Name the blood parasite species.
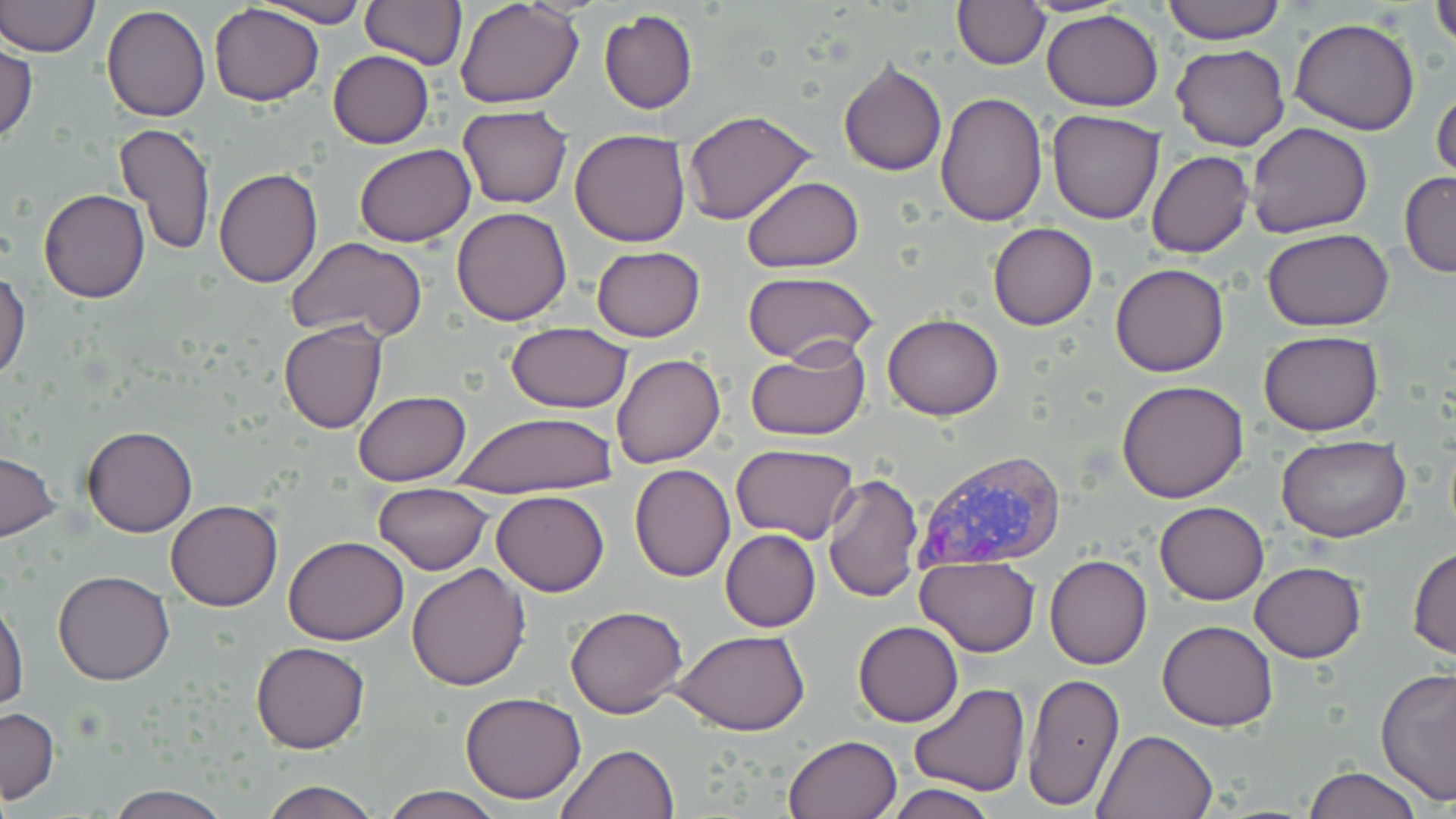
Plasmodium vivax.

Approximate bounding boxes as named x1/y1/x2/y2 corners in pixels. Plasmodium vivax-infected red blood cell locations: (x1=911, y1=447, x2=1068, y2=572). Uninfected red blood cell locations: (x1=1, y1=0, x2=100, y2=57), (x1=1160, y1=0, x2=1286, y2=44), (x1=1432, y1=0, x2=1455, y2=53), (x1=253, y1=1, x2=369, y2=27), (x1=360, y1=1, x2=467, y2=69), (x1=455, y1=1, x2=583, y2=108), (x1=951, y1=1, x2=1050, y2=71), (x1=208, y1=2, x2=324, y2=106), (x1=101, y1=4, x2=210, y2=121), (x1=599, y1=9, x2=698, y2=113), (x1=1041, y1=9, x2=1164, y2=110), (x1=1290, y1=17, x2=1420, y2=135), (x1=1, y1=42, x2=37, y2=142), (x1=1172, y1=42, x2=1291, y2=151), (x1=327, y1=49, x2=434, y2=149), (x1=838, y1=59, x2=947, y2=177), (x1=1431, y1=81, x2=1455, y2=189), (x1=935, y1=93, x2=1048, y2=227), (x1=458, y1=105, x2=573, y2=209), (x1=682, y1=109, x2=817, y2=225), (x1=1046, y1=109, x2=1165, y2=224), (x1=1245, y1=122, x2=1373, y2=240), (x1=114, y1=123, x2=216, y2=256), (x1=568, y1=128, x2=691, y2=246), (x1=354, y1=144, x2=477, y2=247), (x1=1146, y1=150, x2=1253, y2=258), (x1=212, y1=168, x2=323, y2=288), (x1=1399, y1=172, x2=1456, y2=276), (x1=741, y1=177, x2=865, y2=273), (x1=39, y1=187, x2=150, y2=304), (x1=451, y1=206, x2=572, y2=326), (x1=987, y1=222, x2=1098, y2=330), (x1=1262, y1=228, x2=1393, y2=333), (x1=283, y1=237, x2=428, y2=343), (x1=591, y1=245, x2=706, y2=342), (x1=1110, y1=263, x2=1229, y2=377), (x1=1, y1=269, x2=30, y2=381), (x1=743, y1=271, x2=877, y2=363), (x1=882, y1=315, x2=1003, y2=421), (x1=278, y1=322, x2=386, y2=435), (x1=503, y1=322, x2=633, y2=413), (x1=1257, y1=329, x2=1384, y2=437), (x1=746, y1=338, x2=872, y2=441), (x1=611, y1=352, x2=725, y2=467), (x1=1117, y1=379, x2=1249, y2=502), (x1=353, y1=390, x2=470, y2=486), (x1=447, y1=412, x2=616, y2=498), (x1=81, y1=424, x2=198, y2=537), (x1=1278, y1=436, x2=1411, y2=543), (x1=730, y1=443, x2=859, y2=544), (x1=0, y1=450, x2=60, y2=542), (x1=629, y1=464, x2=736, y2=583), (x1=821, y1=470, x2=924, y2=603), (x1=373, y1=483, x2=493, y2=575), (x1=492, y1=490, x2=609, y2=596), (x1=166, y1=500, x2=282, y2=612), (x1=1154, y1=501, x2=1269, y2=604), (x1=720, y1=529, x2=821, y2=632), (x1=283, y1=536, x2=408, y2=645), (x1=1407, y1=545, x2=1456, y2=660), (x1=915, y1=554, x2=1040, y2=655), (x1=1045, y1=555, x2=1151, y2=670), (x1=405, y1=562, x2=531, y2=691), (x1=1250, y1=562, x2=1366, y2=663), (x1=55, y1=569, x2=174, y2=684), (x1=1, y1=594, x2=28, y2=710), (x1=565, y1=603, x2=689, y2=719), (x1=853, y1=620, x2=962, y2=727), (x1=1157, y1=620, x2=1278, y2=731), (x1=673, y1=630, x2=810, y2=735), (x1=250, y1=641, x2=369, y2=754), (x1=1376, y1=666, x2=1455, y2=802), (x1=1023, y1=672, x2=1125, y2=810), (x1=909, y1=683, x2=1031, y2=796), (x1=460, y1=691, x2=585, y2=803), (x1=0, y1=707, x2=58, y2=804), (x1=1092, y1=728, x2=1219, y2=818), (x1=784, y1=734, x2=903, y2=819), (x1=555, y1=744, x2=678, y2=819), (x1=1304, y1=765, x2=1422, y2=819), (x1=257, y1=778, x2=382, y2=818), (x1=881, y1=783, x2=1002, y2=819), (x1=104, y1=784, x2=231, y2=819), (x1=381, y1=786, x2=506, y2=819). Optical microscopy. Image is 1456×819 pixels. May-Grünwald-Giemsa-stained preparation. Thin blood film. Captured at 1000x magnification. Single field of view.